Name the blood parasite species.
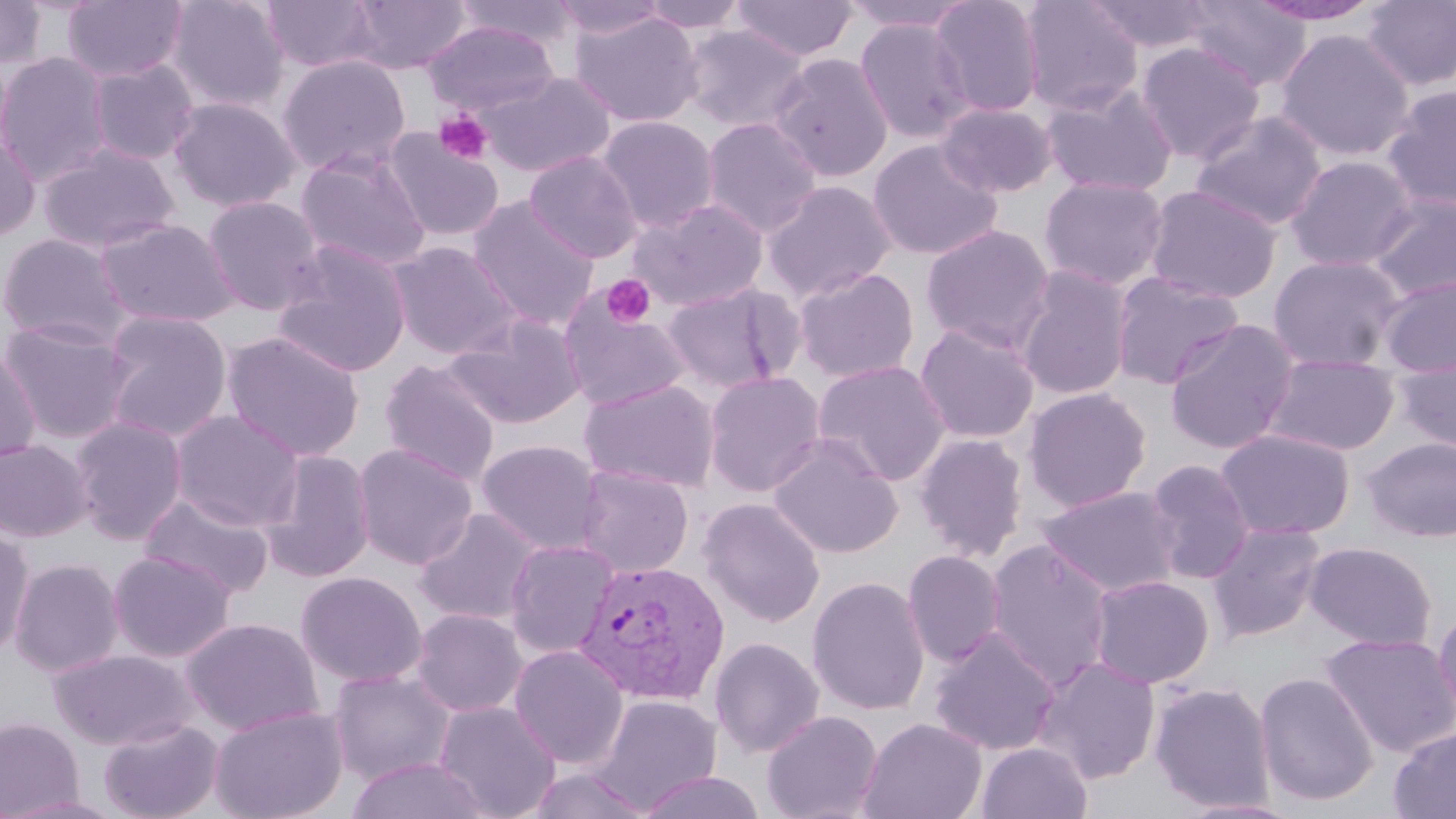
Plasmodium vivax.

Approximate bounding boxes as (x1,y1)-(x2,y2) corner pairs in pixels. Uninfected red blood cell locations: (0,0)-(46,69), (165,0)-(290,114), (261,0)-(383,72), (344,0)-(471,74), (550,0)-(669,42), (636,0)-(753,34), (929,0)-(1044,118), (1018,0)-(1144,116), (1084,0)-(1217,53), (1180,0)-(1312,92), (1247,0)-(1385,26), (1361,0)-(1456,91), (62,1)-(188,82), (453,1)-(579,51), (731,1)-(858,61), (838,1)-(978,32), (569,10)-(704,127), (854,17)-(974,144), (423,20)-(560,117), (680,24)-(810,133), (1275,28)-(1415,162), (1136,41)-(1266,164), (0,51)-(113,184), (768,53)-(894,182), (277,55)-(411,176), (87,60)-(199,165), (479,71)-(615,179), (1040,82)-(1178,197), (1382,85)-(1456,211), (169,97)-(301,213), (936,101)-(1058,198), (1191,111)-(1328,230), (596,115)-(720,233), (701,117)-(822,238), (384,130)-(504,242), (0,132)-(41,242), (868,139)-(1004,261), (38,143)-(180,254), (295,149)-(432,271), (524,150)-(643,263), (1285,155)-(1417,272), (1039,175)-(1169,291), (762,180)-(896,302), (1144,184)-(1283,304), (1367,192)-(1456,300), (202,194)-(326,316), (466,196)-(600,330), (629,198)-(769,311), (96,219)-(239,328), (921,224)-(1055,353), (0,233)-(132,349), (389,241)-(521,359), (272,242)-(412,378), (1268,255)-(1406,371), (793,266)-(919,383), (1014,266)-(1133,401), (1110,270)-(1244,390), (1377,276)-(1456,377), (661,281)-(802,393), (559,294)-(692,412), (102,311)-(232,442), (444,313)-(586,428), (0,319)-(139,445), (1163,319)-(1301,455), (914,323)-(1039,444), (222,331)-(365,462), (0,346)-(41,467), (1262,353)-(1400,456), (1394,354)-(1456,457), (380,359)-(501,486), (813,360)-(951,486), (704,370)-(826,497), (579,379)-(720,492), (1022,387)-(1152,512), (170,410)-(305,531), (69,416)-(189,544), (1216,428)-(1355,541), (914,433)-(1029,562), (768,434)-(903,559), (1362,436)-(1456,543), (0,439)-(93,542), (476,439)-(605,555), (353,443)-(477,569), (259,450)-(375,582), (1144,458)-(1255,584), (573,465)-(694,578), (1038,485)-(1181,598), (138,492)-(274,598), (699,497)-(826,627), (413,508)-(545,626), (1207,521)-(1327,642), (1,524)-(35,658), (985,538)-(1115,690), (504,539)-(618,657), (1305,541)-(1437,651), (107,550)-(235,662), (902,550)-(1006,667), (9,558)-(124,677), (295,571)-(428,688), (1088,574)-(1215,688), (807,576)-(930,716), (411,607)-(528,717), (1431,607)-(1456,726), (180,617)-(323,735), (929,628)-(1061,756), (1320,632)-(1456,758), (709,636)-(825,758), (508,643)-(629,768), (49,648)-(197,750), (1032,656)-(1160,784), (327,669)-(457,786), (1254,671)-(1379,807), (1150,681)-(1276,812), (591,695)-(723,812), (433,700)-(561,818), (209,704)-(349,819), (761,710)-(883,819), (0,717)-(84,817), (98,717)-(224,819), (859,717)-(987,819), (1389,725)-(1456,819), (977,741)-(1093,819), (345,756)-(494,819), (525,765)-(655,819), (635,770)-(768,819), (1174,798)-(1307,818). Platelet locations: (434,110)-(494,165), (602,274)-(655,328). Plasmodium vivax-infected red blood cell locations: (575,560)-(730,705). Light microscopy. Thin blood smear. Image is 1456×819 pixels. May-Grünwald-Giemsa stain. 1000x magnification. Single field of view.